Report the malaria status of this cell.
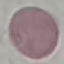
Uninfected.

Summary:
  - Image type: automatically extracted cell patch, resized to 64 × 64 pixels
  - Stain: Giemsa
  - Capture: smartphone camera at the microscope eyepiece
  - Preparation: thin blood film